Identify the cell.
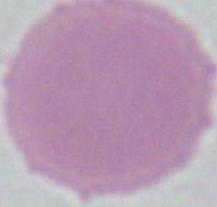

An erythrocyte.

Captured at 1000x magnification. Photomicrograph.